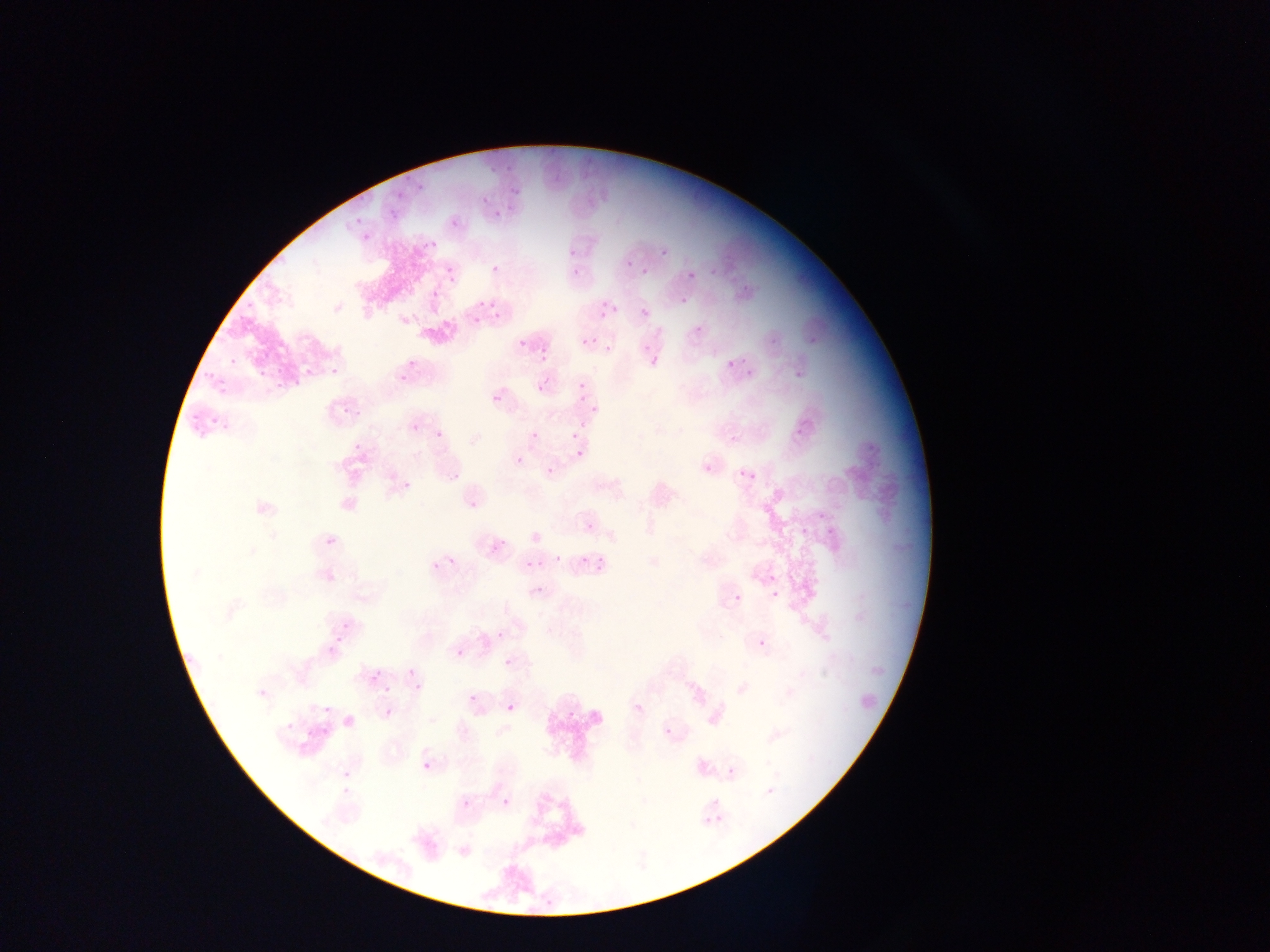
{
  "capture": "mobile-phone photograph through a microscope",
  "image_size": "1270×952 pixels",
  "country": "Ghana",
  "preparation": "thin blood smear",
  "malaria_parasite_locations": "approximate bounding boxes as [left, top, right, bottom] in pixels: [501, 157, 522, 171], [476, 163, 496, 182], [394, 178, 411, 193], [508, 178, 524, 197], [418, 184, 428, 195], [481, 195, 490, 203], [390, 202, 406, 212], [350, 208, 367, 226], [492, 208, 508, 222], [450, 217, 460, 228], [362, 228, 378, 247], [657, 249, 665, 260], [568, 256, 586, 275], [490, 260, 501, 276], [625, 260, 634, 269], [445, 266, 456, 278], [641, 269, 649, 278], [684, 269, 701, 284], [739, 282, 748, 297], [485, 287, 502, 304], [680, 299, 688, 305], [588, 301, 602, 320], [609, 305, 619, 315], [640, 307, 650, 317], [470, 312, 482, 326], [495, 317, 503, 329], [694, 323, 708, 332], [806, 335, 819, 349], [641, 339, 657, 352], [583, 340, 596, 349], [514, 343, 523, 354], [604, 345, 613, 353], [405, 346, 419, 370], [532, 351, 552, 362], [719, 353, 737, 370], [742, 357, 757, 382], [228, 360, 238, 367], [792, 363, 806, 383], [331, 364, 340, 378], [270, 365, 293, 384], [198, 367, 210, 384], [247, 367, 264, 389], [299, 367, 313, 378], [528, 372, 549, 396], [213, 374, 233, 393], [398, 374, 412, 385], [575, 380, 584, 389], [285, 381, 297, 394], [493, 394, 503, 404], [576, 400, 587, 406], [342, 401, 354, 412], [590, 402, 600, 415], [208, 415, 223, 429], [410, 423, 421, 432], [436, 431, 443, 440], [531, 432, 539, 441], [571, 433, 578, 442], [730, 434, 740, 444], [352, 442, 363, 452], [576, 450, 584, 458], [515, 456, 523, 464], [546, 467, 553, 476], [738, 469, 748, 479], [790, 518, 813, 537], [821, 522, 837, 539], [322, 540, 344, 553], [554, 554, 563, 563], [447, 556, 457, 565], [578, 557, 586, 565], [524, 560, 533, 570], [325, 570, 336, 580], [768, 573, 778, 582], [534, 586, 546, 595], [770, 589, 779, 598], [733, 594, 742, 602], [339, 619, 349, 629], [758, 639, 767, 648], [456, 649, 466, 659], [504, 658, 512, 667], [406, 667, 415, 676], [370, 672, 381, 683], [414, 682, 423, 693], [384, 684, 393, 693], [467, 694, 476, 703], [318, 701, 333, 720], [634, 702, 643, 712], [507, 704, 515, 712], [384, 708, 394, 717], [279, 712, 298, 736], [663, 727, 672, 737], [305, 729, 316, 740], [423, 763, 431, 770], [727, 767, 734, 775], [348, 775, 360, 784], [767, 787, 774, 795], [501, 798, 510, 808]",
  "field_of_view": "single"
}